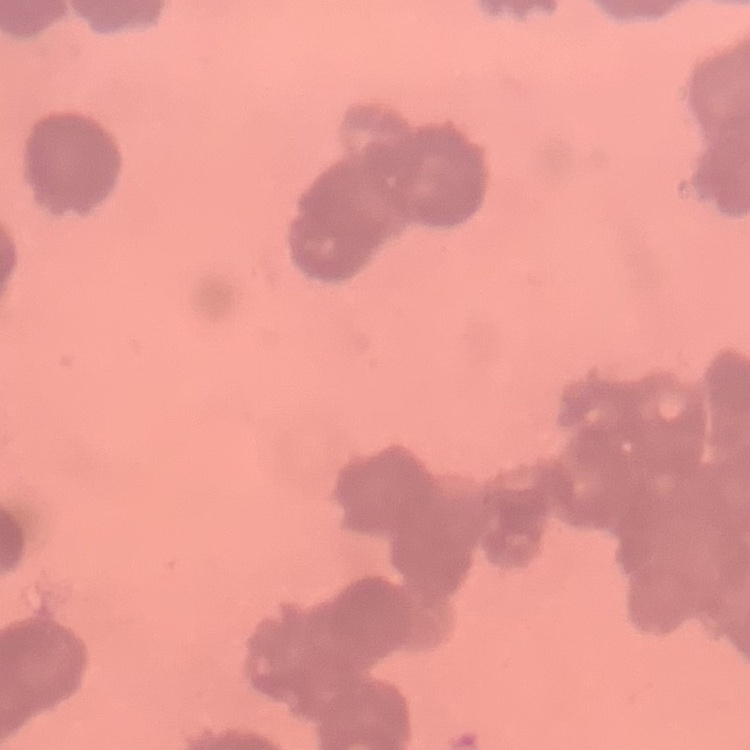
Summary:
  - Red blood cell morphology: rouleaux formation
  - Image type: one tile cut from a larger photomicrograph
  - Preparation: thin blood smear
  - Stain: Field's or Giemsa